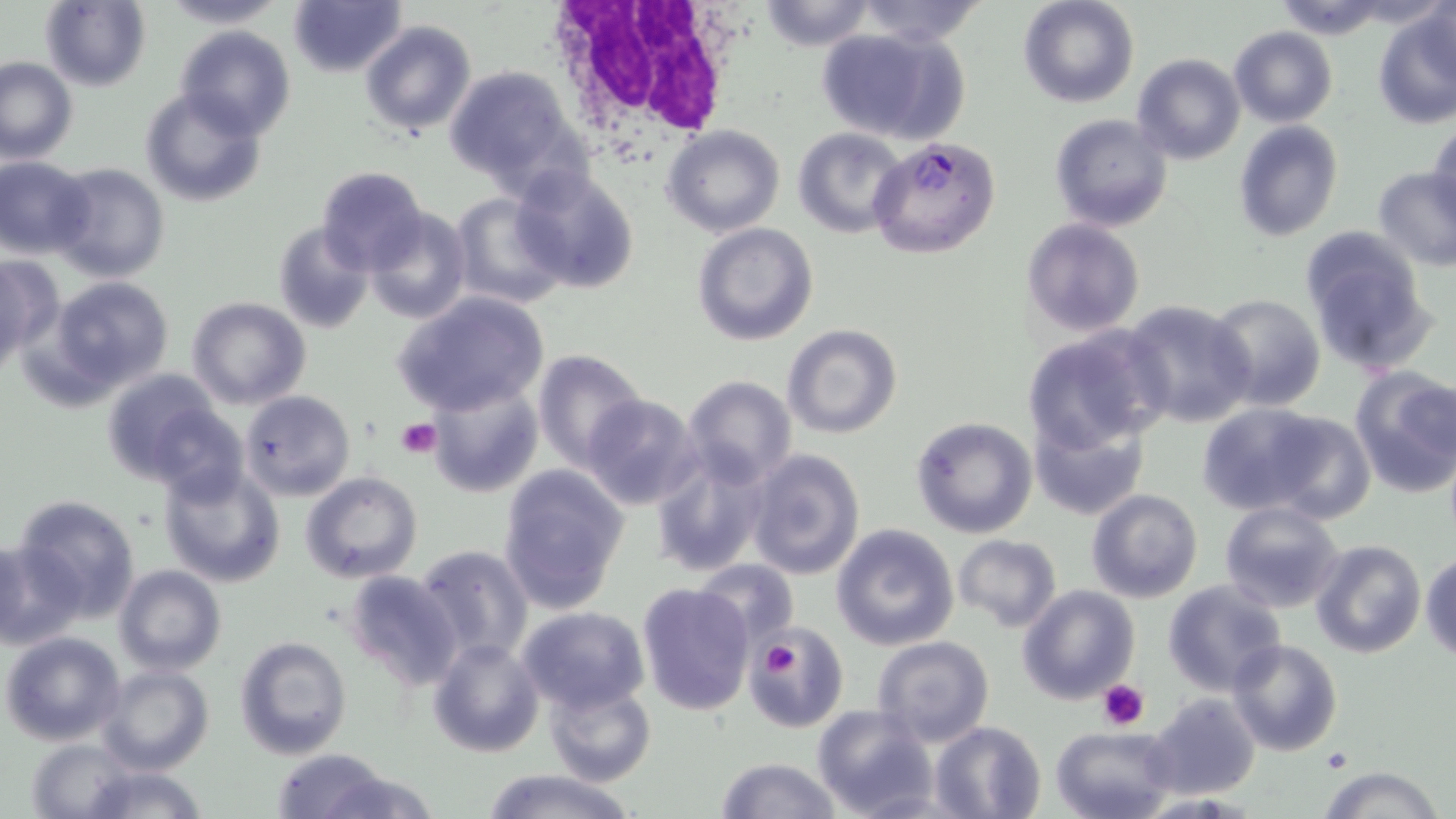

Approximate bounding boxes as named x1/y1/x2/y2 corners in pixels. Uninfected red blood cell locations: (x1=41, y1=0, x2=151, y2=91), (x1=158, y1=0, x2=288, y2=28), (x1=289, y1=0, x2=408, y2=77), (x1=756, y1=0, x2=877, y2=49), (x1=855, y1=0, x2=984, y2=46), (x1=1017, y1=0, x2=1139, y2=108), (x1=1268, y1=0, x2=1396, y2=42), (x1=1372, y1=10, x2=1455, y2=127), (x1=359, y1=20, x2=476, y2=138), (x1=174, y1=26, x2=296, y2=138), (x1=812, y1=27, x2=967, y2=147), (x1=1229, y1=27, x2=1337, y2=126), (x1=1132, y1=54, x2=1245, y2=166), (x1=1, y1=56, x2=78, y2=165), (x1=444, y1=65, x2=584, y2=190), (x1=140, y1=86, x2=267, y2=208), (x1=1049, y1=113, x2=1174, y2=233), (x1=1233, y1=120, x2=1343, y2=241), (x1=1428, y1=121, x2=1455, y2=226), (x1=662, y1=124, x2=786, y2=238), (x1=793, y1=127, x2=907, y2=236), (x1=1, y1=156, x2=94, y2=257), (x1=48, y1=161, x2=170, y2=284), (x1=315, y1=164, x2=429, y2=273), (x1=510, y1=165, x2=642, y2=295), (x1=1372, y1=166, x2=1456, y2=271), (x1=449, y1=193, x2=571, y2=310), (x1=364, y1=207, x2=471, y2=323), (x1=1020, y1=218, x2=1146, y2=337), (x1=272, y1=221, x2=374, y2=335), (x1=692, y1=223, x2=820, y2=347), (x1=1299, y1=229, x2=1436, y2=375), (x1=0, y1=251, x2=59, y2=372), (x1=50, y1=276, x2=175, y2=392), (x1=1204, y1=292, x2=1327, y2=412), (x1=393, y1=293, x2=550, y2=416), (x1=186, y1=296, x2=311, y2=409), (x1=1119, y1=299, x2=1258, y2=428), (x1=783, y1=324, x2=903, y2=440), (x1=1021, y1=327, x2=1165, y2=453), (x1=532, y1=349, x2=650, y2=472), (x1=1350, y1=367, x2=1456, y2=496), (x1=101, y1=368, x2=233, y2=488), (x1=683, y1=376, x2=797, y2=488), (x1=428, y1=380, x2=545, y2=498), (x1=240, y1=391, x2=355, y2=500), (x1=581, y1=395, x2=704, y2=511), (x1=1193, y1=400, x2=1353, y2=518), (x1=149, y1=405, x2=247, y2=507), (x1=1029, y1=412, x2=1150, y2=522), (x1=910, y1=416, x2=1038, y2=538), (x1=648, y1=445, x2=770, y2=575), (x1=746, y1=446, x2=866, y2=581), (x1=158, y1=461, x2=288, y2=589), (x1=499, y1=466, x2=630, y2=611), (x1=299, y1=472, x2=422, y2=585), (x1=1087, y1=489, x2=1203, y2=603), (x1=12, y1=493, x2=143, y2=621), (x1=1219, y1=501, x2=1347, y2=615), (x1=831, y1=522, x2=960, y2=650), (x1=953, y1=534, x2=1060, y2=632), (x1=0, y1=539, x2=84, y2=649), (x1=1310, y1=539, x2=1428, y2=658), (x1=414, y1=543, x2=535, y2=665), (x1=1420, y1=551, x2=1456, y2=662), (x1=690, y1=560, x2=799, y2=653), (x1=115, y1=565, x2=226, y2=676), (x1=344, y1=569, x2=462, y2=691), (x1=1162, y1=580, x2=1286, y2=694), (x1=638, y1=581, x2=756, y2=717), (x1=1018, y1=585, x2=1140, y2=703), (x1=516, y1=606, x2=651, y2=713), (x1=745, y1=626, x2=849, y2=731), (x1=1, y1=632, x2=125, y2=746), (x1=234, y1=634, x2=354, y2=760), (x1=871, y1=637, x2=994, y2=748), (x1=427, y1=638, x2=544, y2=757), (x1=1226, y1=638, x2=1343, y2=756), (x1=99, y1=666, x2=213, y2=776), (x1=546, y1=681, x2=656, y2=786), (x1=1147, y1=692, x2=1261, y2=801), (x1=812, y1=705, x2=938, y2=819), (x1=930, y1=721, x2=1046, y2=818), (x1=1050, y1=726, x2=1177, y2=819), (x1=25, y1=737, x2=143, y2=816), (x1=269, y1=748, x2=392, y2=819), (x1=714, y1=757, x2=841, y2=818), (x1=68, y1=761, x2=214, y2=819), (x1=1320, y1=765, x2=1444, y2=819), (x1=320, y1=768, x2=437, y2=819), (x1=473, y1=769, x2=638, y2=819). Platelet locations: (x1=398, y1=419, x2=441, y2=459), (x1=757, y1=640, x2=798, y2=681), (x1=1097, y1=680, x2=1149, y2=730), (x1=1321, y1=749, x2=1351, y2=772). White blood cell locations: (x1=543, y1=3, x2=735, y2=150). Plasmodium falciparum-infected red blood cell locations: (x1=867, y1=137, x2=1001, y2=257). Slide-level diagnosis: Plasmodium falciparum. Optical microscopy. May-Grünwald-Giemsa-stained preparation. Single field of view. Thin blood smear. 1000x magnification. Image is 1456×819 pixels.